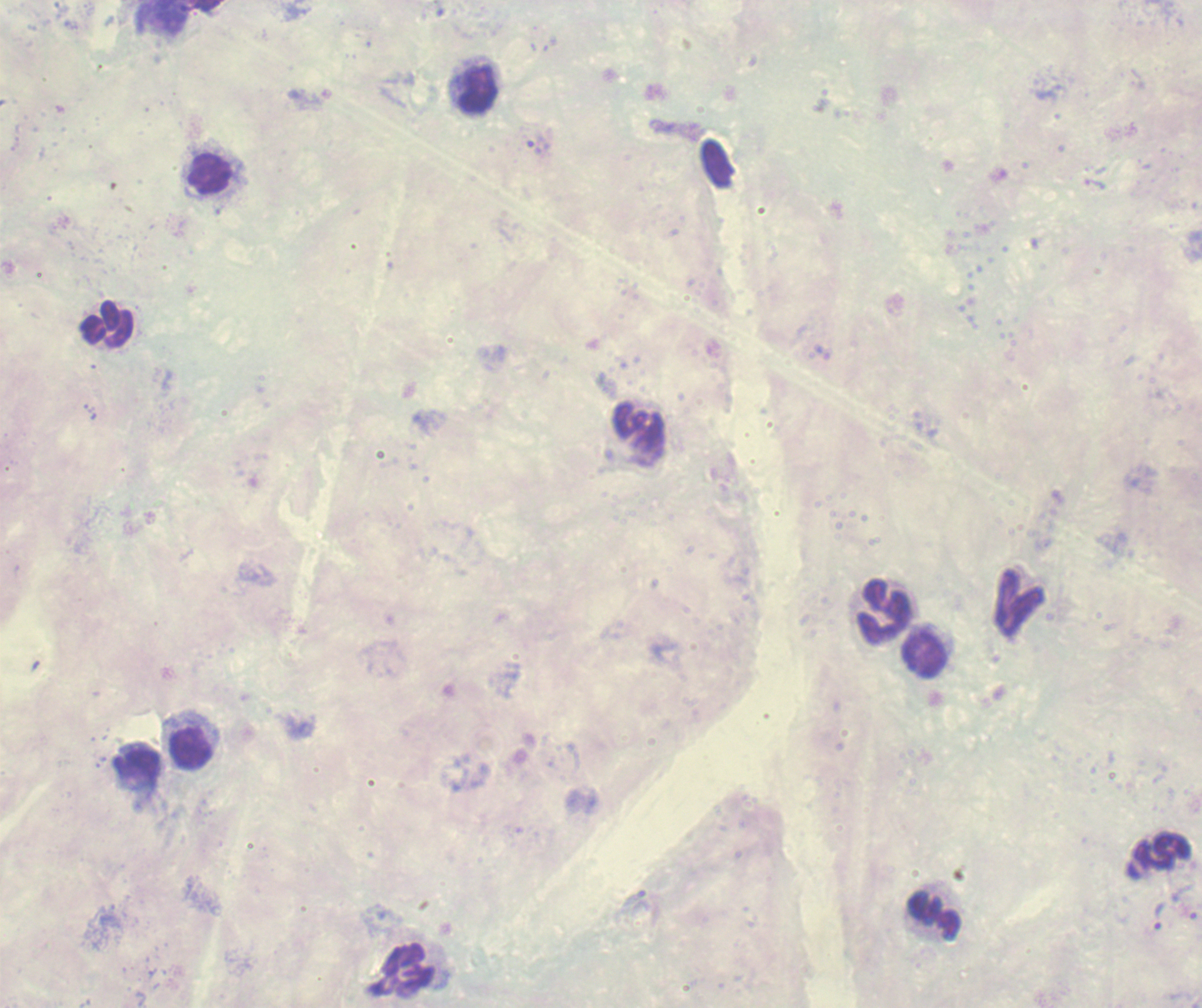
Approximate centers as {x, y} in pixels.
Summary:
  - Trophozoite locations: {1159, 914}
  - Leukocyte locations: {477, 89}, {211, 177}, {105, 324}, {639, 430}, {1019, 603}, {883, 611}, {925, 654}, {190, 747}, {136, 766}, {1158, 855}, {933, 915}, {401, 969}
  - Image size: 1202×1008 pixels
  - Stain: Romanowsky
  - Context: previously used in a real diagnosis
  - Result: Plasmodium parasites detected
  - Preparation: thick blood smear
  - Magnification: 100x
  - Background quality: unsatisfactory
  - Field of view: single